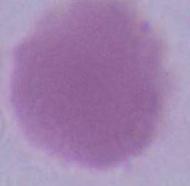
Captured at 1000x magnification. A red blood cell is seen. Photomicrograph.